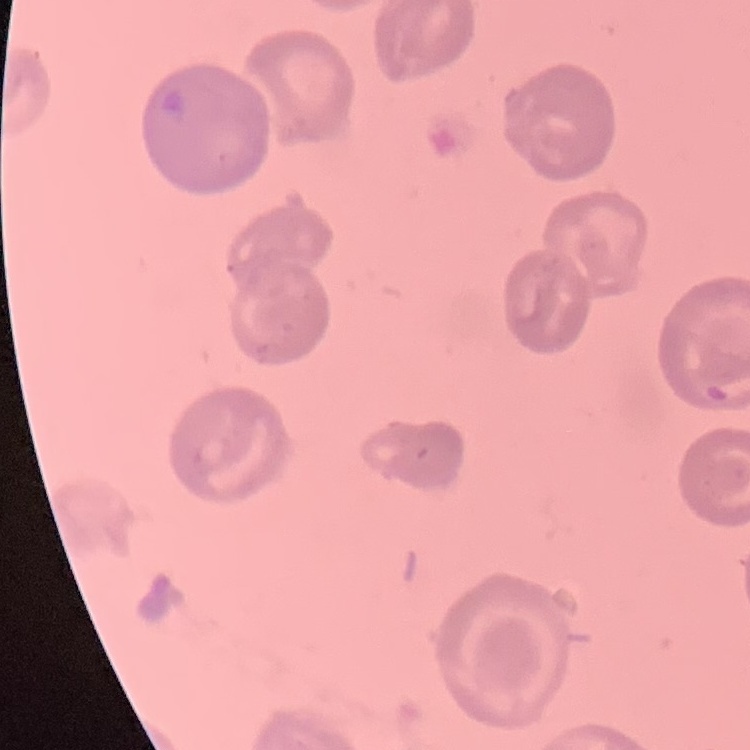
red_blood_cell_morphology: no rouleaux formation
image_type: one tile cut from a larger photomicrograph
stain: Field's or Giemsa
preparation: thin peripheral smear